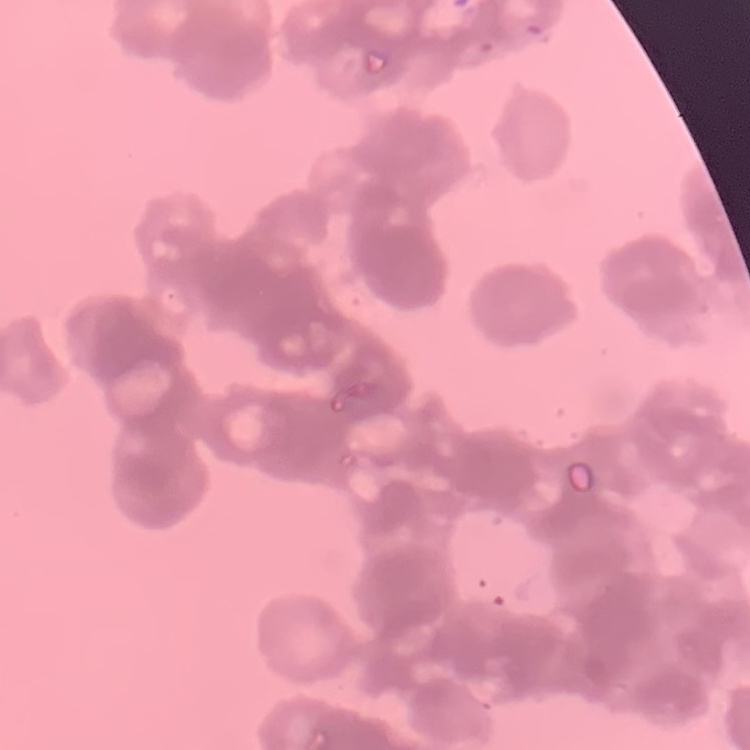
The red blood cells show rouleaux formation. Thin blood film. Stained with either Field's or Giemsa. One tile cut from a larger photomicrograph.